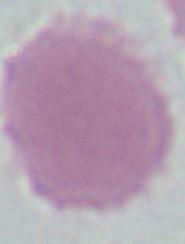

Captured at 1000x magnification. A red blood cell is seen. Micrograph.